Assess the morphology of the red blood cells.
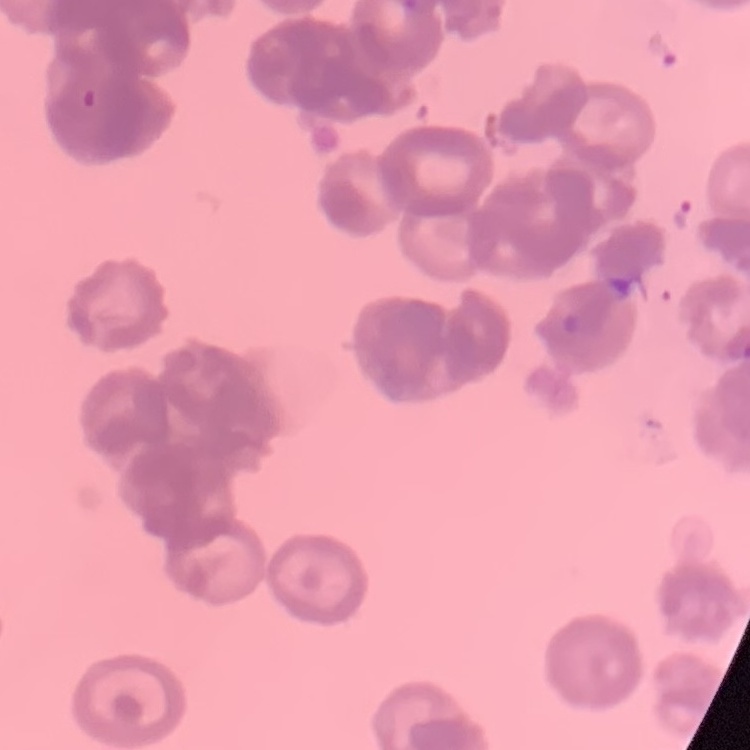
Rouleaux formation.

Thin blood film. Field's or Giemsa stain. One tile cut from a larger photomicrograph.